Classify this cell by malaria status.
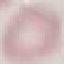
Uninfected.

Summary:
  - Stain: Giemsa
  - Capture: smartphone camera at the microscope eyepiece
  - Preparation: thin smear
  - Image type: automatically extracted cell patch, resized to 64 × 64 pixels